Name the parasite shown.
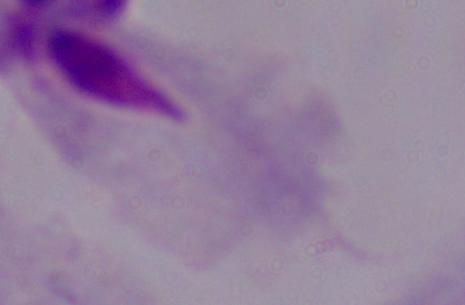

This is a trichomonad.

Summary:
  - Modality: micrograph
  - Magnification: 1000x